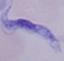

magnification = 1000x
identification = trypanosome
modality = photomicrograph